Locate every malaria parasite and every leukocyte.
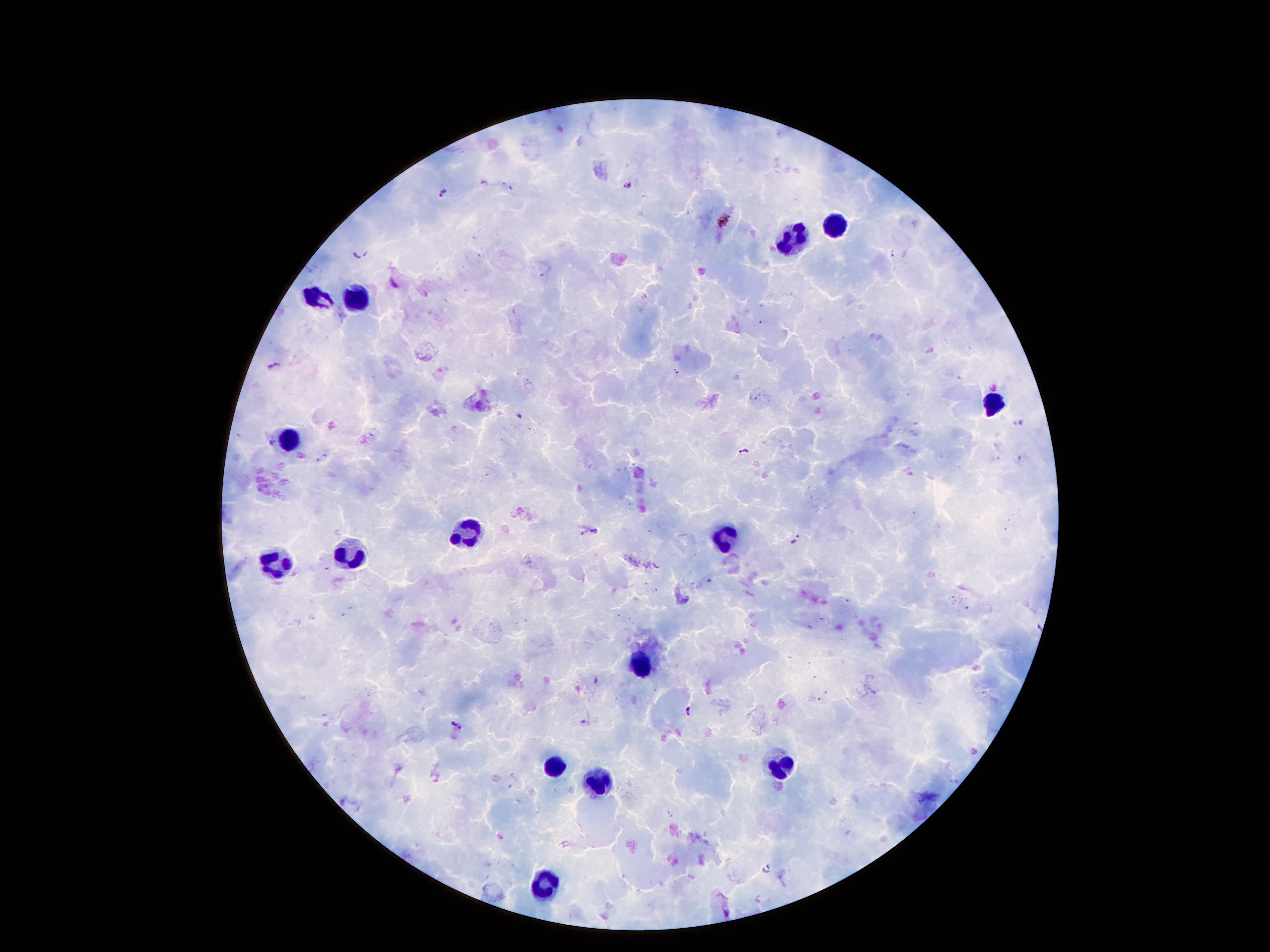

Approximate centers as [x, y] in pixels.
Malaria parasites: [626, 185], [442, 193], [725, 222], [359, 253], [276, 366], [677, 371], [519, 416], [743, 451], [793, 539], [689, 713], [457, 726], [769, 868].
Leukocytes: [836, 224], [793, 246], [312, 296], [363, 300], [992, 400], [290, 438], [465, 532], [724, 542], [351, 554], [276, 563], [638, 662], [551, 766], [781, 769], [597, 783], [547, 880].

patient malaria status = infected with Plasmodium falciparum
field of view = one from this slide
image size = 1270×952 pixels
stain = Giemsa
magnification = 100x
preparation = thick blood smear
capture = smartphone through the microscope eyepiece